Name the parasite shown.
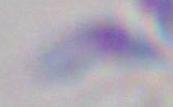

This is Toxoplasma gondii.

Micrograph. Captured at 1000x magnification.